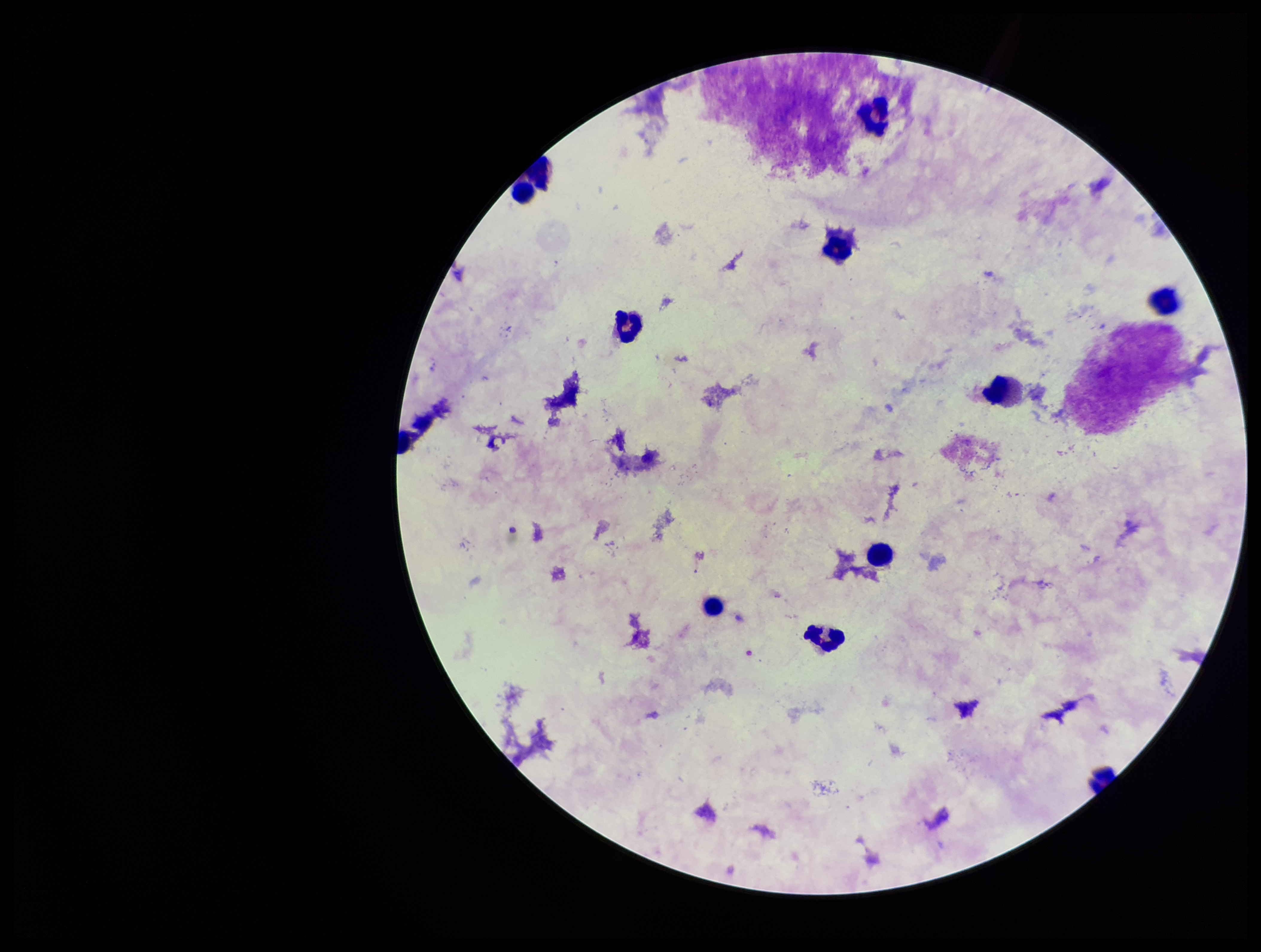

{
  "leukocyte_count": 9,
  "stain": "Giemsa",
  "plasmodium_parasites": "none seen",
  "image_size": "1261×952 pixels",
  "patient_malaria_status": "negative",
  "capture": "smartphone photograph through the microscope eyepiece",
  "field_of_view": "one from this slide",
  "parasite_count": 0,
  "preparation": "thick"
}